Report the malaria status of this cell.
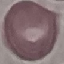
It is uninfected.

Acquired by smartphone through the microscope eyepiece. Cell patch, automatically extracted from a larger field of view and resized to 64 × 64 pixels. Giemsa stain. Thin smear of blood.